Comment on the morphology of the erythrocytes.
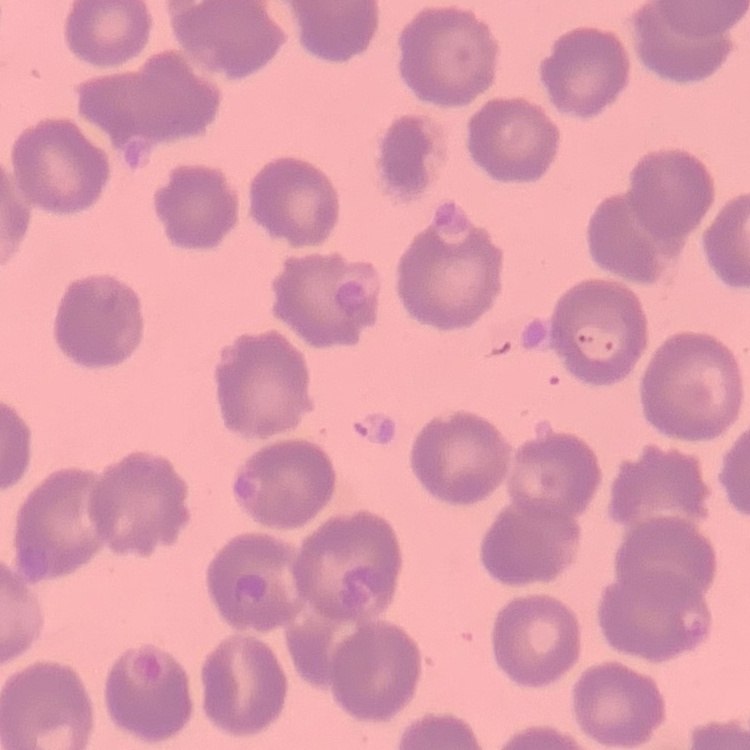
No rouleaux formation.

stain = Field's or Giemsa
preparation = thin peripheral smear
image type = one tile cut from a larger photomicrograph